State which cell type is depicted.
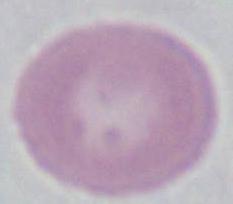

This is an erythrocyte.

Summary:
  - Magnification: 1000x
  - Modality: photomicrograph